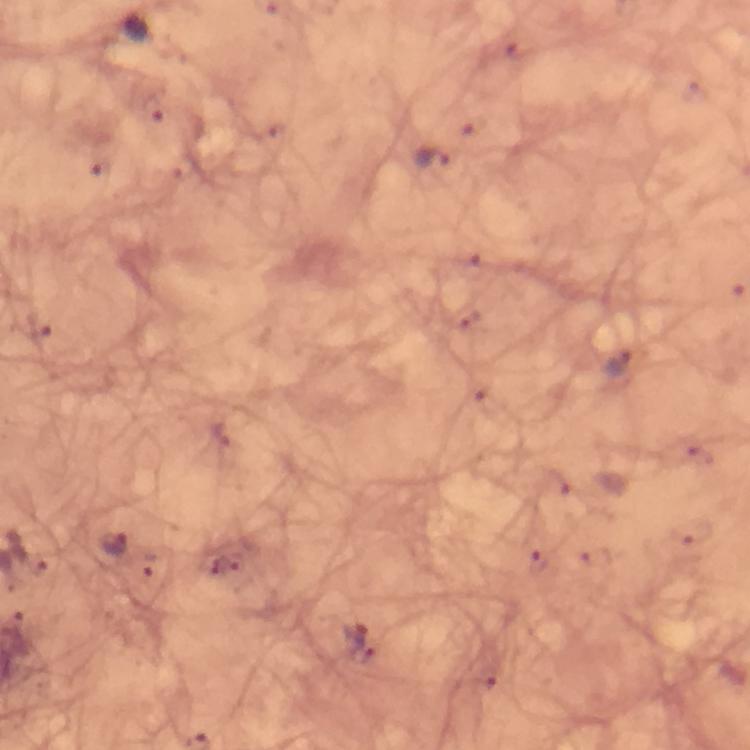
Approximate object centers, in pixels from the top-left corner. Malaria parasite locations: (x=434, y=159), (x=618, y=363), (x=112, y=544), (x=352, y=638). Immersion oil was used. Thick blood smear. Photographed with a smartphone mounted on the microscope. From a malaria diagnostic workup. Giemsa stain. A crop from one field of view. Image is 750×750 pixels. 100x magnification.